Locate every Plasmodium falciparum-infected red blood cell.
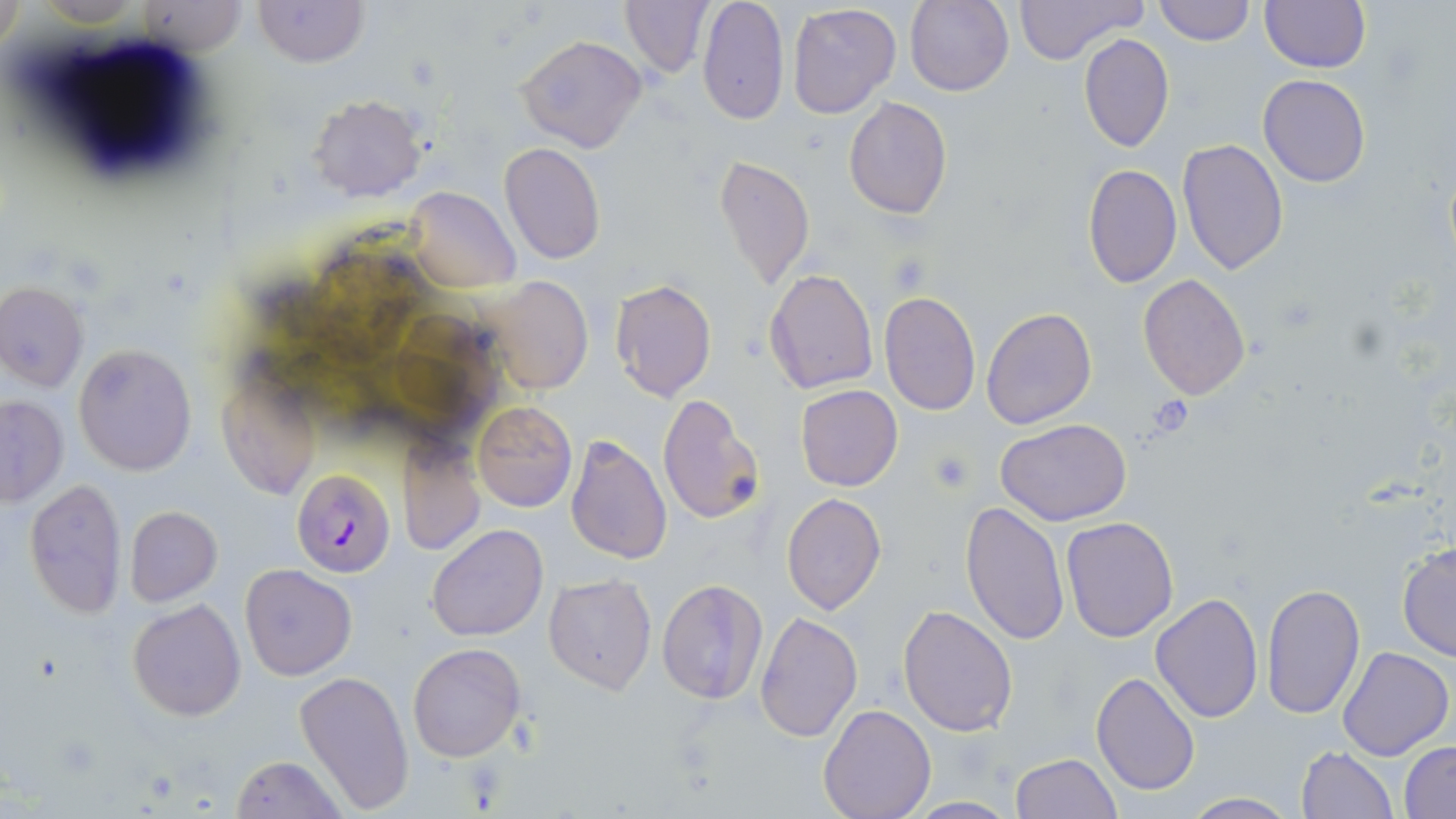
Approximate bounding boxes as named x1/y1/x2/y2 corners in pixels.
Plasmodium falciparum-infected red blood cells: (x1=292, y1=469, x2=395, y2=576).

slide-level diagnosis = Plasmodium falciparum
platelet locations = approximate bounding boxes as named x1/y1/x2/y2 corners in pixels: (x1=1144, y1=392, x2=1197, y2=436)
modality = light microscopy
field of view = single
image size = 1456×819 pixels
stain = May-Grünwald-Giemsa
preparation = thin blood film
magnification = 1000x
uninfected red blood cell locations = approximate bounding boxes as named x1/y1/x2/y2 corners in pixels: (x1=255, y1=0, x2=366, y2=67), (x1=619, y1=0, x2=714, y2=77), (x1=905, y1=0, x2=1014, y2=97), (x1=1012, y1=0, x2=1147, y2=64), (x1=140, y1=1, x2=245, y2=57), (x1=695, y1=1, x2=789, y2=125), (x1=1153, y1=1, x2=1254, y2=45), (x1=1261, y1=1, x2=1370, y2=73), (x1=786, y1=2, x2=901, y2=118), (x1=1078, y1=33, x2=1174, y2=152), (x1=514, y1=34, x2=647, y2=152), (x1=1258, y1=75, x2=1370, y2=187), (x1=308, y1=94, x2=426, y2=202), (x1=843, y1=97, x2=952, y2=220), (x1=1177, y1=139, x2=1289, y2=273), (x1=499, y1=141, x2=606, y2=265), (x1=713, y1=154, x2=815, y2=291), (x1=1082, y1=164, x2=1182, y2=289), (x1=406, y1=186, x2=519, y2=292), (x1=765, y1=269, x2=878, y2=395), (x1=1137, y1=273, x2=1251, y2=400), (x1=483, y1=275, x2=593, y2=394), (x1=608, y1=278, x2=718, y2=402), (x1=0, y1=283, x2=88, y2=393), (x1=878, y1=290, x2=981, y2=416), (x1=981, y1=307, x2=1098, y2=429), (x1=73, y1=344, x2=197, y2=476), (x1=215, y1=372, x2=322, y2=499), (x1=796, y1=384, x2=903, y2=491), (x1=655, y1=393, x2=765, y2=526), (x1=0, y1=395, x2=67, y2=506), (x1=472, y1=401, x2=576, y2=512), (x1=996, y1=419, x2=1131, y2=527), (x1=565, y1=436, x2=673, y2=566), (x1=398, y1=438, x2=484, y2=557), (x1=24, y1=476, x2=128, y2=618), (x1=781, y1=492, x2=886, y2=615), (x1=959, y1=501, x2=1069, y2=648), (x1=124, y1=506, x2=222, y2=605), (x1=1061, y1=517, x2=1179, y2=640), (x1=428, y1=524, x2=546, y2=641), (x1=1396, y1=541, x2=1456, y2=662), (x1=240, y1=564, x2=356, y2=679), (x1=543, y1=573, x2=657, y2=694), (x1=656, y1=578, x2=768, y2=704), (x1=1261, y1=582, x2=1366, y2=719), (x1=1151, y1=592, x2=1263, y2=723), (x1=127, y1=598, x2=246, y2=722), (x1=897, y1=605, x2=1018, y2=738), (x1=756, y1=612, x2=862, y2=741), (x1=408, y1=642, x2=526, y2=763), (x1=1336, y1=647, x2=1453, y2=761), (x1=294, y1=670, x2=415, y2=810), (x1=1091, y1=672, x2=1199, y2=795), (x1=819, y1=704, x2=936, y2=819), (x1=1400, y1=742, x2=1456, y2=817), (x1=1297, y1=747, x2=1397, y2=819), (x1=1011, y1=753, x2=1122, y2=818), (x1=231, y1=755, x2=347, y2=818), (x1=1181, y1=792, x2=1298, y2=818), (x1=902, y1=796, x2=1021, y2=817)